Locate every Plasmodium falciparum-infected red blood cell.
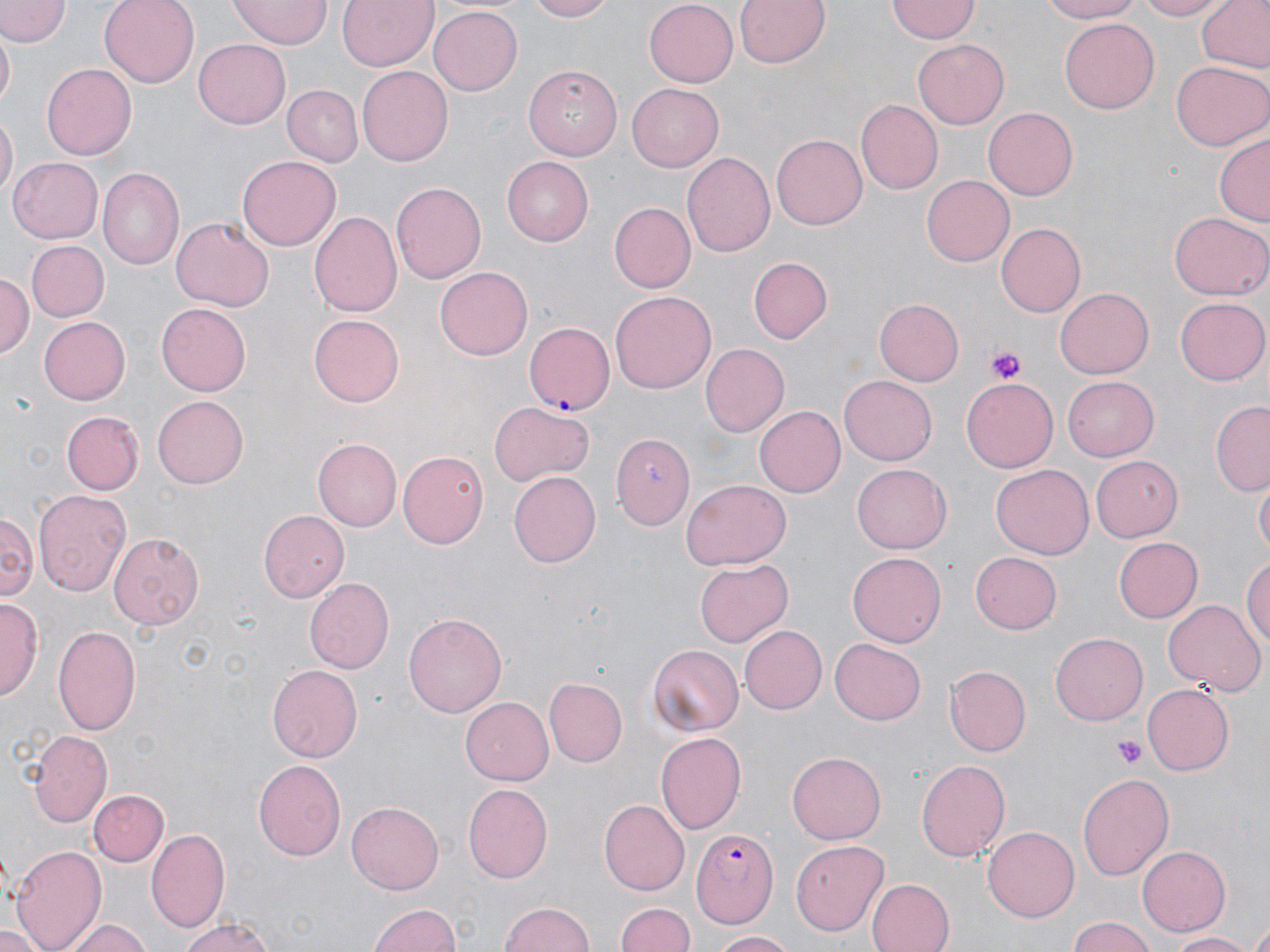

Approximate bounding boxes as named x1/y1/x2/y2 corners in pixels.
Plasmodium falciparum-infected red blood cells: (x1=524, y1=322, x2=615, y2=415), (x1=691, y1=829, x2=779, y2=928).

Summary:
  - Platelet locations: (x1=985, y1=347, x2=1029, y2=385), (x1=1115, y1=734, x2=1146, y2=770)
  - Uninfected red blood cell locations: (x1=0, y1=0, x2=66, y2=47), (x1=100, y1=0, x2=199, y2=87), (x1=338, y1=0, x2=438, y2=70), (x1=523, y1=0, x2=614, y2=22), (x1=644, y1=0, x2=737, y2=85), (x1=733, y1=0, x2=832, y2=70), (x1=1036, y1=0, x2=1146, y2=23), (x1=1134, y1=0, x2=1227, y2=21), (x1=1196, y1=0, x2=1270, y2=75), (x1=230, y1=1, x2=332, y2=46), (x1=887, y1=1, x2=978, y2=43), (x1=428, y1=8, x2=523, y2=96), (x1=1059, y1=19, x2=1161, y2=115), (x1=1, y1=32, x2=15, y2=109), (x1=193, y1=40, x2=291, y2=128), (x1=913, y1=40, x2=1009, y2=130), (x1=41, y1=60, x2=136, y2=158), (x1=1170, y1=60, x2=1270, y2=151), (x1=357, y1=65, x2=453, y2=166), (x1=523, y1=66, x2=623, y2=161), (x1=282, y1=83, x2=363, y2=165), (x1=627, y1=83, x2=724, y2=171), (x1=855, y1=101, x2=941, y2=194), (x1=983, y1=106, x2=1078, y2=200), (x1=1, y1=115, x2=17, y2=203), (x1=1215, y1=132, x2=1270, y2=228), (x1=771, y1=134, x2=867, y2=229), (x1=682, y1=152, x2=776, y2=258), (x1=500, y1=155, x2=593, y2=245), (x1=238, y1=156, x2=341, y2=251), (x1=7, y1=157, x2=102, y2=243), (x1=97, y1=169, x2=182, y2=270), (x1=922, y1=176, x2=1014, y2=267), (x1=390, y1=180, x2=487, y2=286), (x1=611, y1=201, x2=696, y2=292), (x1=310, y1=209, x2=402, y2=320), (x1=1170, y1=212, x2=1269, y2=301), (x1=172, y1=217, x2=273, y2=312), (x1=995, y1=222, x2=1085, y2=317), (x1=25, y1=240, x2=109, y2=321), (x1=749, y1=257, x2=833, y2=344), (x1=435, y1=267, x2=531, y2=360), (x1=0, y1=271, x2=33, y2=360), (x1=1055, y1=286, x2=1153, y2=376), (x1=609, y1=291, x2=716, y2=396), (x1=1176, y1=296, x2=1269, y2=385), (x1=873, y1=298, x2=966, y2=386), (x1=157, y1=304, x2=250, y2=396), (x1=308, y1=314, x2=404, y2=407), (x1=38, y1=315, x2=131, y2=405), (x1=700, y1=343, x2=788, y2=436), (x1=840, y1=374, x2=939, y2=464), (x1=1060, y1=374, x2=1158, y2=464), (x1=961, y1=376, x2=1058, y2=475), (x1=152, y1=395, x2=246, y2=488), (x1=488, y1=401, x2=597, y2=485), (x1=1211, y1=402, x2=1269, y2=495), (x1=754, y1=405, x2=846, y2=497), (x1=62, y1=411, x2=143, y2=494), (x1=612, y1=429, x2=696, y2=529), (x1=311, y1=437, x2=402, y2=531), (x1=399, y1=451, x2=490, y2=548), (x1=1090, y1=455, x2=1183, y2=543), (x1=852, y1=464, x2=951, y2=555), (x1=990, y1=464, x2=1093, y2=559), (x1=509, y1=471, x2=601, y2=567), (x1=682, y1=479, x2=791, y2=569), (x1=1254, y1=480, x2=1268, y2=558), (x1=33, y1=490, x2=131, y2=598), (x1=2, y1=509, x2=36, y2=601), (x1=259, y1=510, x2=352, y2=604), (x1=110, y1=534, x2=207, y2=628), (x1=1114, y1=536, x2=1202, y2=623), (x1=970, y1=549, x2=1062, y2=633), (x1=848, y1=551, x2=945, y2=648), (x1=1243, y1=553, x2=1270, y2=653), (x1=695, y1=560, x2=793, y2=646), (x1=306, y1=578, x2=397, y2=673), (x1=2, y1=597, x2=41, y2=703), (x1=1164, y1=599, x2=1263, y2=696), (x1=404, y1=612, x2=504, y2=718), (x1=53, y1=623, x2=142, y2=735), (x1=740, y1=626, x2=827, y2=713), (x1=1051, y1=633, x2=1148, y2=724), (x1=829, y1=638, x2=926, y2=725), (x1=646, y1=644, x2=742, y2=735), (x1=266, y1=664, x2=363, y2=762), (x1=946, y1=665, x2=1031, y2=756), (x1=543, y1=678, x2=625, y2=769), (x1=1142, y1=684, x2=1235, y2=775), (x1=461, y1=697, x2=556, y2=785), (x1=27, y1=728, x2=112, y2=826), (x1=657, y1=732, x2=745, y2=834), (x1=788, y1=753, x2=885, y2=845), (x1=914, y1=757, x2=1009, y2=861), (x1=253, y1=759, x2=346, y2=862), (x1=1078, y1=773, x2=1173, y2=880), (x1=464, y1=783, x2=555, y2=882), (x1=90, y1=789, x2=169, y2=866), (x1=347, y1=800, x2=443, y2=894), (x1=598, y1=800, x2=689, y2=896), (x1=983, y1=826, x2=1079, y2=920), (x1=146, y1=831, x2=229, y2=935), (x1=790, y1=838, x2=890, y2=937), (x1=9, y1=844, x2=107, y2=952), (x1=1138, y1=845, x2=1230, y2=936), (x1=866, y1=878, x2=954, y2=952), (x1=497, y1=902, x2=598, y2=951), (x1=615, y1=902, x2=694, y2=952), (x1=367, y1=903, x2=464, y2=952), (x1=1245, y1=914, x2=1270, y2=952), (x1=1065, y1=915, x2=1157, y2=952), (x1=65, y1=917, x2=151, y2=952), (x1=179, y1=917, x2=281, y2=952), (x1=0, y1=925, x2=51, y2=952), (x1=1165, y1=930, x2=1259, y2=950), (x1=709, y1=931, x2=799, y2=950)
  - Slide-level diagnosis: Plasmodium falciparum
  - Stain: May-Grünwald-Giemsa
  - Modality: light microscopy
  - Magnification: 1000x
  - Image size: 1270×952 pixels
  - Field of view: single
  - Preparation: thin blood film